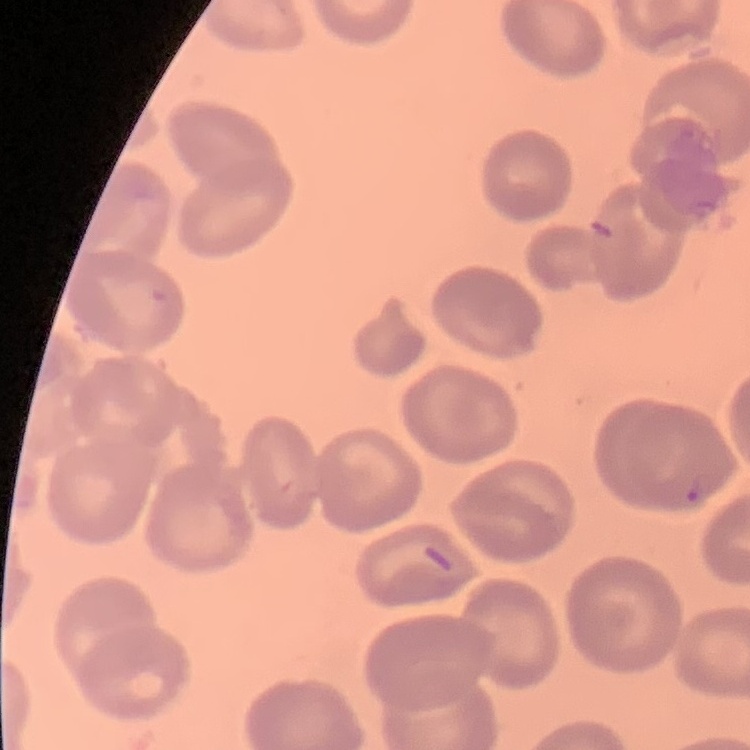
{
  "red_blood_cell_morphology": "no rouleaux formation",
  "stain": "Field's or Giemsa",
  "image_type": "one tile cut from a larger photomicrograph",
  "preparation": "thin blood film"
}